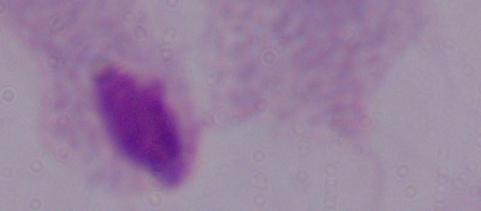
Summary:
  - Modality: photomicrograph
  - Identification: trichomonad
  - Magnification: 1000x